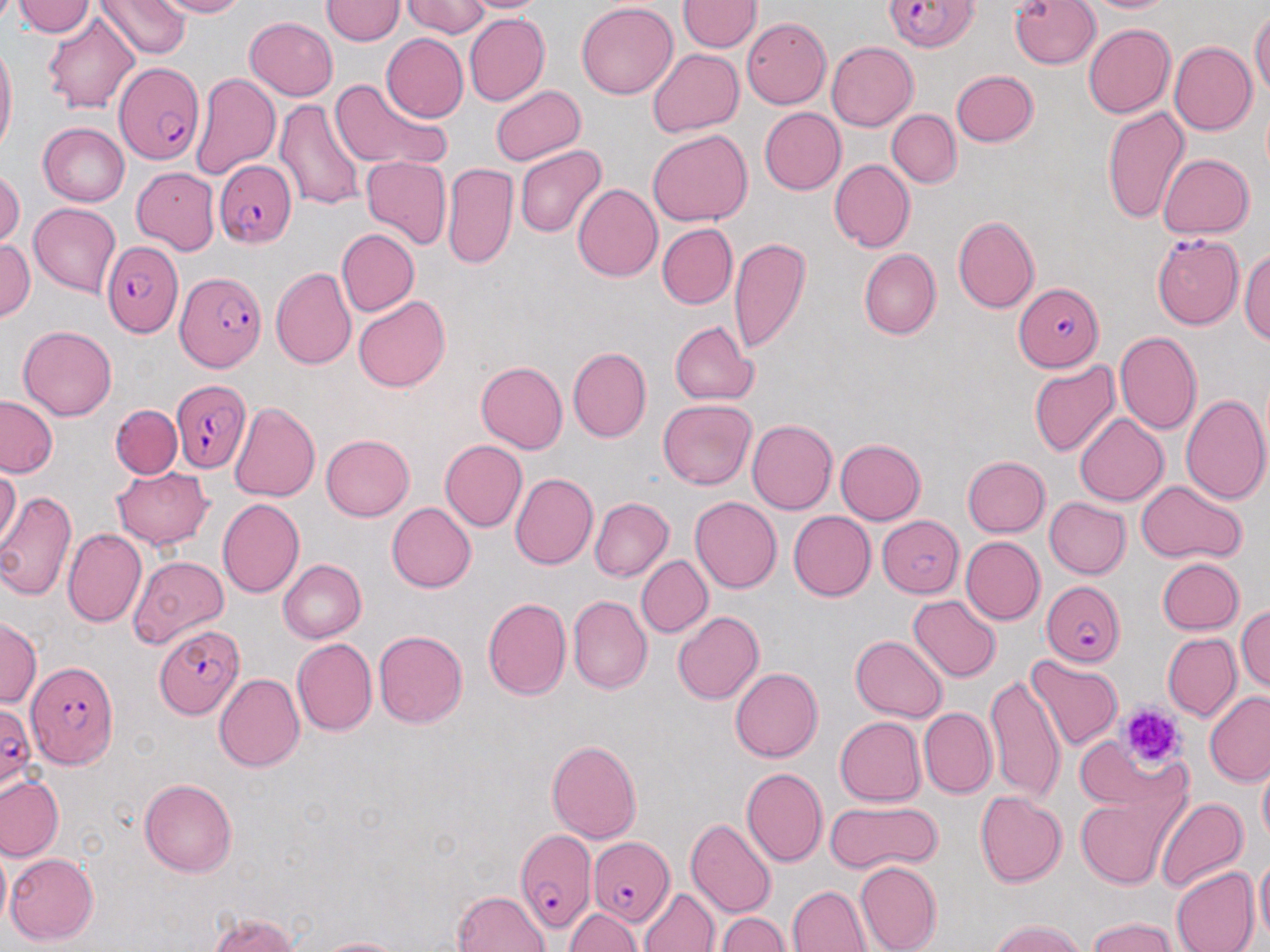
Approximate bounding boxes as named x1/y1/x2/y2 corners in pixels. Uninfected red blood cell locations: (x1=13, y1=0, x2=96, y2=38), (x1=99, y1=0, x2=189, y2=60), (x1=151, y1=0, x2=251, y2=18), (x1=399, y1=0, x2=490, y2=38), (x1=461, y1=0, x2=546, y2=16), (x1=1009, y1=0, x2=1102, y2=71), (x1=1083, y1=0, x2=1179, y2=16), (x1=680, y1=1, x2=761, y2=54), (x1=322, y1=2, x2=404, y2=46), (x1=574, y1=3, x2=679, y2=100), (x1=1250, y1=7, x2=1269, y2=102), (x1=1013, y1=9, x2=1170, y2=85), (x1=41, y1=13, x2=140, y2=112), (x1=462, y1=14, x2=552, y2=108), (x1=741, y1=16, x2=830, y2=105), (x1=244, y1=17, x2=338, y2=100), (x1=1083, y1=22, x2=1175, y2=119), (x1=379, y1=33, x2=467, y2=123), (x1=827, y1=41, x2=920, y2=132), (x1=1168, y1=42, x2=1256, y2=137), (x1=0, y1=43, x2=16, y2=157), (x1=645, y1=47, x2=742, y2=139), (x1=949, y1=69, x2=1038, y2=149), (x1=192, y1=72, x2=279, y2=181), (x1=328, y1=79, x2=448, y2=174), (x1=488, y1=82, x2=586, y2=167), (x1=276, y1=96, x2=369, y2=215), (x1=1100, y1=104, x2=1189, y2=225), (x1=757, y1=107, x2=845, y2=195), (x1=888, y1=109, x2=960, y2=189), (x1=39, y1=123, x2=130, y2=206), (x1=647, y1=129, x2=753, y2=227), (x1=515, y1=144, x2=607, y2=238), (x1=1158, y1=152, x2=1256, y2=239), (x1=362, y1=156, x2=451, y2=249), (x1=829, y1=160, x2=913, y2=251), (x1=132, y1=163, x2=227, y2=259), (x1=442, y1=163, x2=517, y2=269), (x1=0, y1=170, x2=22, y2=246), (x1=573, y1=182, x2=662, y2=282), (x1=28, y1=203, x2=120, y2=296), (x1=951, y1=215, x2=1039, y2=314), (x1=657, y1=224, x2=736, y2=308), (x1=337, y1=228, x2=419, y2=317), (x1=0, y1=235, x2=34, y2=328), (x1=728, y1=236, x2=812, y2=355), (x1=1242, y1=245, x2=1270, y2=350), (x1=858, y1=248, x2=940, y2=341), (x1=269, y1=266, x2=355, y2=369), (x1=353, y1=295, x2=451, y2=392), (x1=670, y1=322, x2=758, y2=404), (x1=17, y1=326, x2=118, y2=421), (x1=1115, y1=332, x2=1201, y2=434), (x1=567, y1=347, x2=651, y2=442), (x1=1028, y1=360, x2=1118, y2=459), (x1=475, y1=361, x2=568, y2=453), (x1=1181, y1=391, x2=1269, y2=505), (x1=0, y1=396, x2=62, y2=477), (x1=658, y1=398, x2=757, y2=489), (x1=231, y1=401, x2=320, y2=501), (x1=111, y1=405, x2=182, y2=479), (x1=1073, y1=413, x2=1167, y2=506), (x1=748, y1=419, x2=840, y2=514), (x1=320, y1=433, x2=416, y2=521), (x1=836, y1=438, x2=926, y2=524), (x1=438, y1=439, x2=528, y2=532), (x1=962, y1=456, x2=1051, y2=537), (x1=1, y1=465, x2=21, y2=546), (x1=110, y1=465, x2=215, y2=549), (x1=510, y1=472, x2=595, y2=569), (x1=1135, y1=481, x2=1248, y2=565), (x1=0, y1=489, x2=78, y2=605), (x1=1043, y1=495, x2=1129, y2=578), (x1=217, y1=497, x2=305, y2=600), (x1=590, y1=497, x2=671, y2=582), (x1=690, y1=497, x2=782, y2=594), (x1=389, y1=501, x2=477, y2=592), (x1=787, y1=510, x2=875, y2=599), (x1=878, y1=516, x2=963, y2=597), (x1=63, y1=528, x2=146, y2=628), (x1=963, y1=537, x2=1044, y2=623), (x1=130, y1=554, x2=229, y2=645), (x1=636, y1=554, x2=712, y2=638), (x1=1157, y1=556, x2=1243, y2=634), (x1=277, y1=558, x2=366, y2=642), (x1=484, y1=594, x2=572, y2=701), (x1=568, y1=594, x2=652, y2=695), (x1=909, y1=595, x2=1001, y2=683), (x1=1235, y1=604, x2=1270, y2=693), (x1=674, y1=611, x2=764, y2=706), (x1=0, y1=620, x2=41, y2=709), (x1=373, y1=628, x2=467, y2=729), (x1=1163, y1=634, x2=1240, y2=724), (x1=851, y1=635, x2=945, y2=722), (x1=293, y1=638, x2=377, y2=736), (x1=1025, y1=656, x2=1122, y2=751), (x1=729, y1=667, x2=823, y2=761), (x1=986, y1=670, x2=1068, y2=803), (x1=214, y1=672, x2=305, y2=773), (x1=1204, y1=691, x2=1270, y2=786), (x1=921, y1=708, x2=994, y2=796), (x1=835, y1=715, x2=925, y2=807), (x1=545, y1=737, x2=643, y2=844), (x1=1077, y1=745, x2=1196, y2=808), (x1=741, y1=767, x2=827, y2=869), (x1=1256, y1=767, x2=1270, y2=845), (x1=1, y1=775, x2=63, y2=861), (x1=138, y1=777, x2=239, y2=875), (x1=976, y1=791, x2=1067, y2=886), (x1=1075, y1=793, x2=1177, y2=888), (x1=1154, y1=795, x2=1245, y2=893), (x1=822, y1=802, x2=940, y2=872), (x1=688, y1=818, x2=775, y2=918), (x1=6, y1=852, x2=98, y2=945), (x1=1254, y1=854, x2=1269, y2=948), (x1=853, y1=861, x2=942, y2=952), (x1=1169, y1=868, x2=1258, y2=952), (x1=788, y1=884, x2=870, y2=952), (x1=639, y1=887, x2=718, y2=952), (x1=451, y1=889, x2=549, y2=952), (x1=564, y1=906, x2=640, y2=952), (x1=718, y1=909, x2=792, y2=952), (x1=204, y1=911, x2=308, y2=952), (x1=1085, y1=919, x2=1182, y2=952), (x1=986, y1=922, x2=1094, y2=952), (x1=314, y1=935, x2=408, y2=952). Plasmodium falciparum-infected red blood cell locations: (x1=880, y1=0, x2=980, y2=52), (x1=117, y1=58, x2=204, y2=170), (x1=216, y1=160, x2=295, y2=249), (x1=1151, y1=235, x2=1242, y2=328), (x1=99, y1=237, x2=180, y2=343), (x1=172, y1=266, x2=266, y2=373), (x1=1010, y1=283, x2=1102, y2=372), (x1=171, y1=378, x2=252, y2=472), (x1=1041, y1=580, x2=1126, y2=667), (x1=155, y1=621, x2=246, y2=719), (x1=25, y1=658, x2=119, y2=770), (x1=0, y1=697, x2=39, y2=791), (x1=512, y1=822, x2=591, y2=938), (x1=587, y1=837, x2=672, y2=927). Platelet locations: (x1=1119, y1=704, x2=1182, y2=776). Slide-level diagnosis: Plasmodium falciparum. 1000x magnification. Thin blood smear. Light microscopy. Image is 1270×952 pixels. Single field of view. May-Grünwald-Giemsa stain.